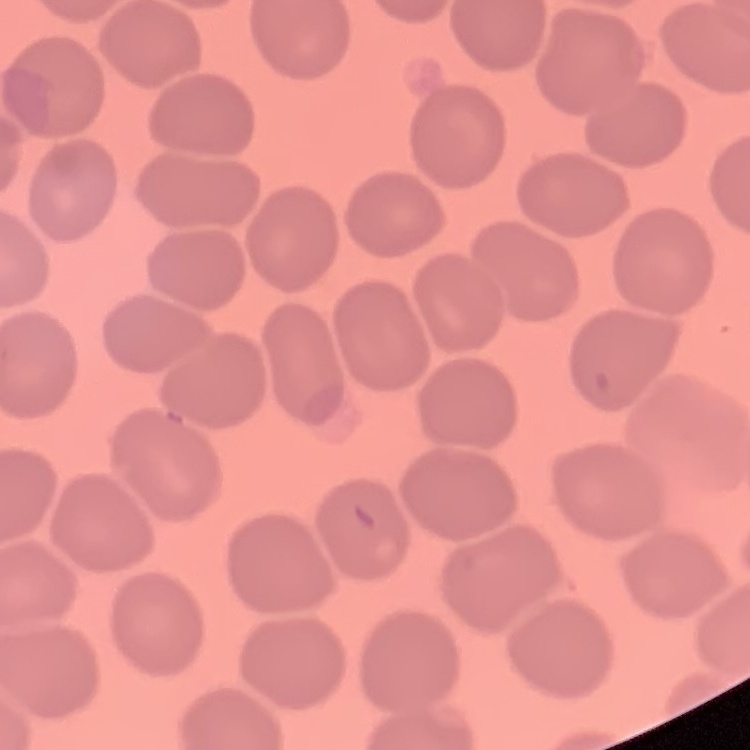

red blood cell morphology = no rouleaux formation
stain = Field's or Giemsa
preparation = thin blood film
image type = square crop of a larger photomicrograph